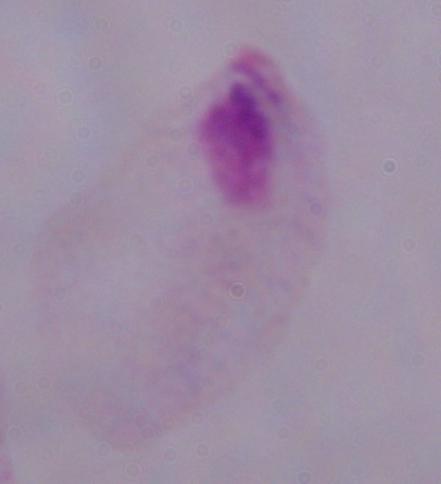 1000x magnification. Photomicrograph. A trichomonad is shown.